Give the position of every malaria parasite.
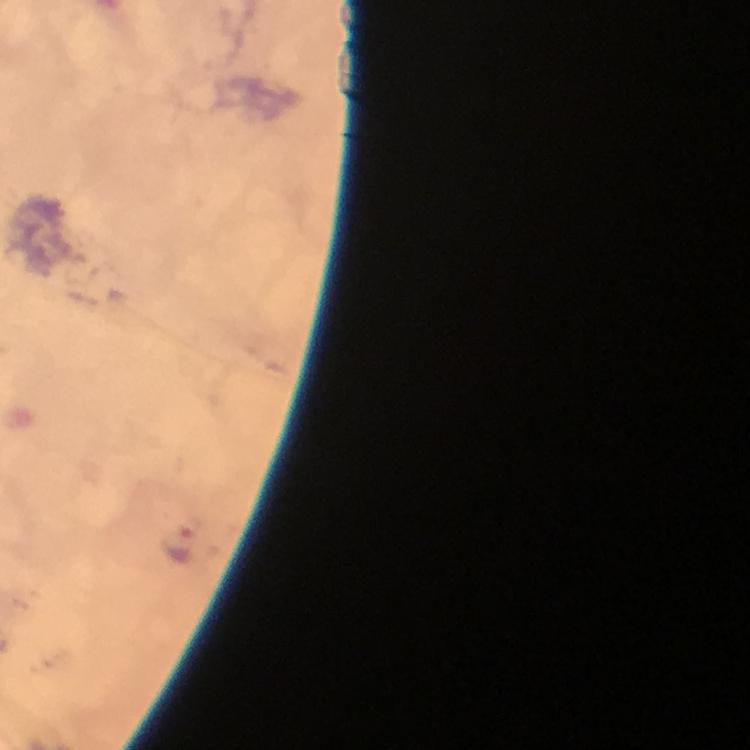

Approximate object centers, in pixels from the top-left corner.
Malaria parasites: (x=179, y=546).

From a malaria diagnostic workup. Immersion oil was used. A crop from one field of view. Image is 750×750 pixels. Thick blood film. At 100x magnification. Giemsa stain. Photographed with a smartphone mounted on the microscope.